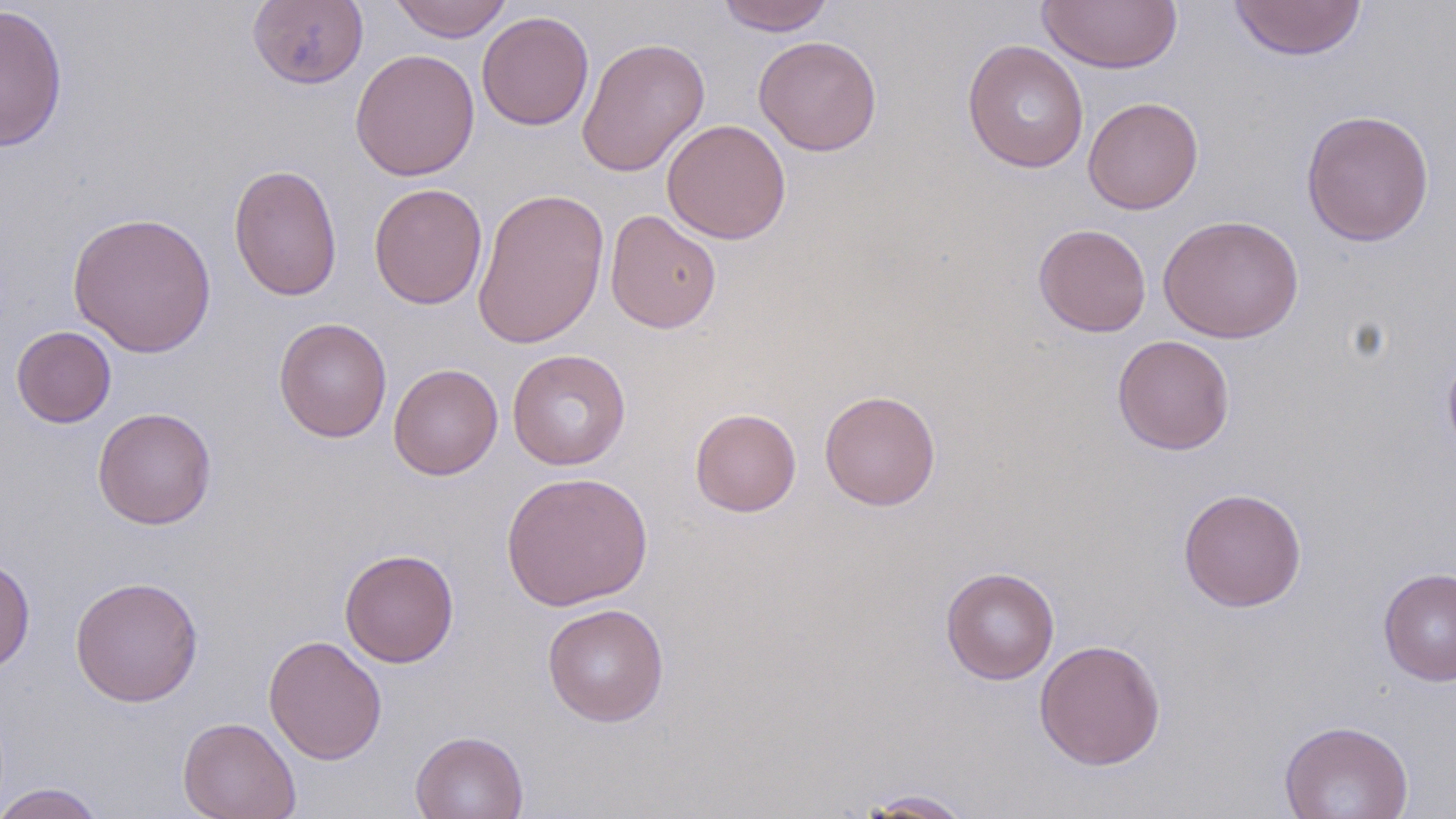
Summary:
  - Coordinate format: approximate bounding boxes as (x1, y1, x2, y2) in pixels
  - Uninfected red blood cell locations: (248, 0, 368, 89), (389, 0, 513, 42), (716, 0, 835, 35), (1038, 1, 1182, 73), (1228, 1, 1367, 61), (0, 4, 68, 151), (476, 11, 595, 131), (754, 35, 882, 157), (576, 36, 710, 177), (962, 40, 1089, 173), (350, 49, 481, 181), (1082, 96, 1204, 215), (1300, 109, 1435, 247), (661, 119, 792, 244), (227, 163, 342, 301), (369, 182, 488, 309), (471, 187, 610, 350), (605, 210, 722, 334), (66, 211, 217, 358), (1157, 214, 1304, 343), (1033, 223, 1152, 337), (274, 317, 392, 443), (11, 326, 116, 428), (1112, 334, 1235, 455), (1442, 345, 1456, 465), (507, 349, 631, 470), (388, 362, 503, 480), (819, 390, 941, 510), (92, 407, 217, 529), (689, 408, 802, 517), (501, 471, 653, 611), (1178, 486, 1307, 612), (339, 549, 459, 668), (0, 554, 35, 676), (940, 567, 1060, 685), (1378, 567, 1456, 686), (70, 575, 203, 707), (542, 603, 669, 726), (263, 634, 387, 765), (1034, 638, 1166, 770), (177, 715, 302, 819), (1279, 719, 1414, 819), (409, 730, 528, 819), (0, 783, 109, 818), (859, 788, 976, 818)
  - Slide-level diagnosis: no evidence of blood parasites
  - Image size: 1456×819 pixels
  - Field of view: single
  - Magnification: 1000x
  - Stain: May-Grünwald-Giemsa
  - Preparation: thin blood film
  - Modality: optical microscopy